Evaluate for malaria.
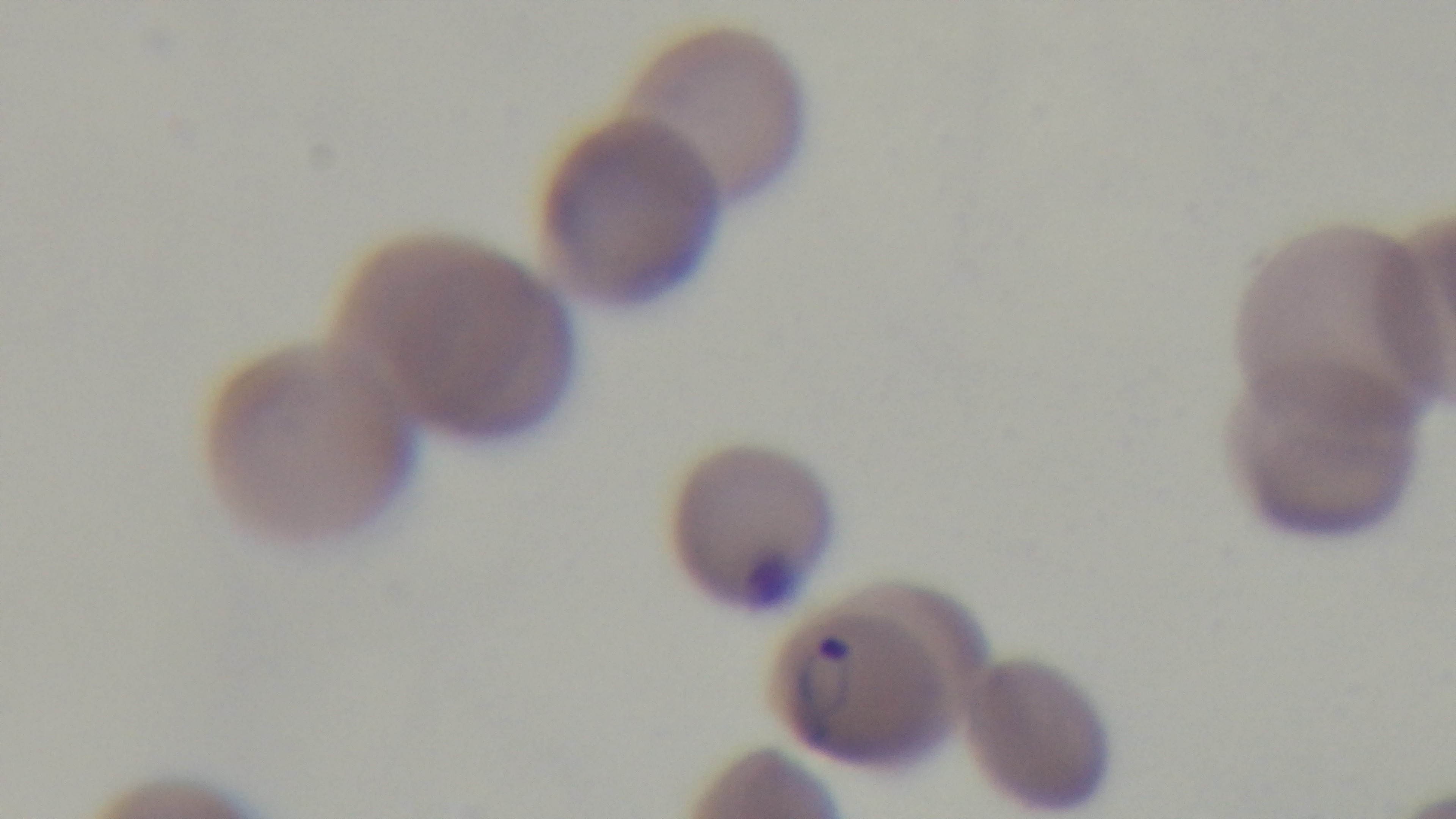

Positive.

Summary:
  - Stain: Giemsa
  - Modality: light microscopy
  - Objective: 100x oil immersion
  - Field of view: single
  - Capture: mounted 4K digital camera
  - Preparation: thin